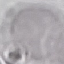 Malaria status: uninfected. Cell patch, automatically extracted from a larger field of view and resized to 64 × 64 pixels. Giemsa-stained preparation. Acquired by smartphone through the microscope eyepiece. Thin blood smear.